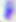

Summary:
  - Identification: Toxoplasma gondii
  - Magnification: 400x
  - Modality: micrograph